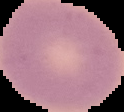

result: no malaria parasites detected
preparation: thin blood film
image_size: 124×112 pixels
image_type: segmented cell region on a black background